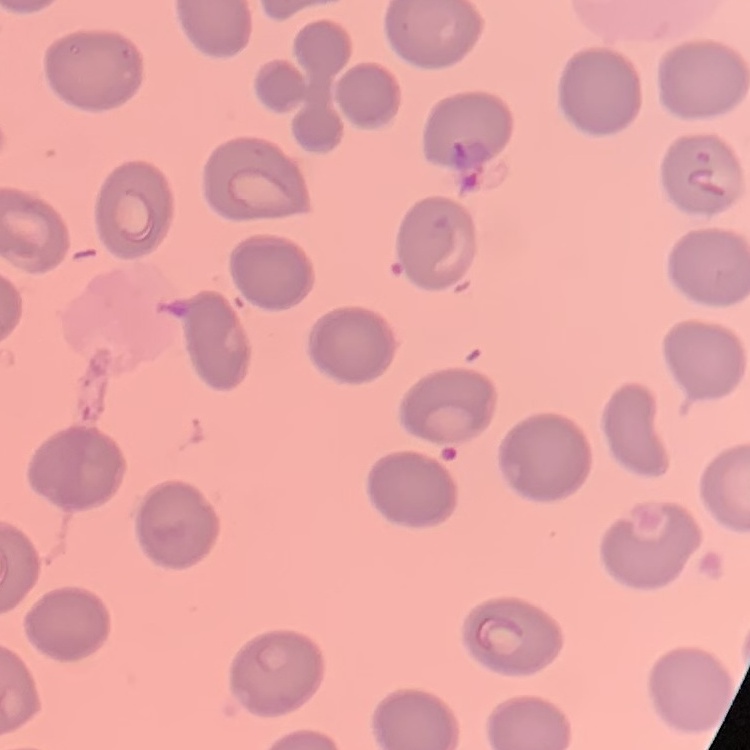

red blood cell morphology = no rouleaux formation
preparation = thin blood film
stain = Field's or Giemsa
image type = square crop of a larger photomicrograph